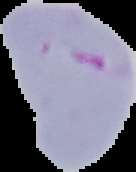

Malaria status: parasitized. From a thin blood smear. Image is 136×172 pixels. The area outside the segmented cell region is set to black.